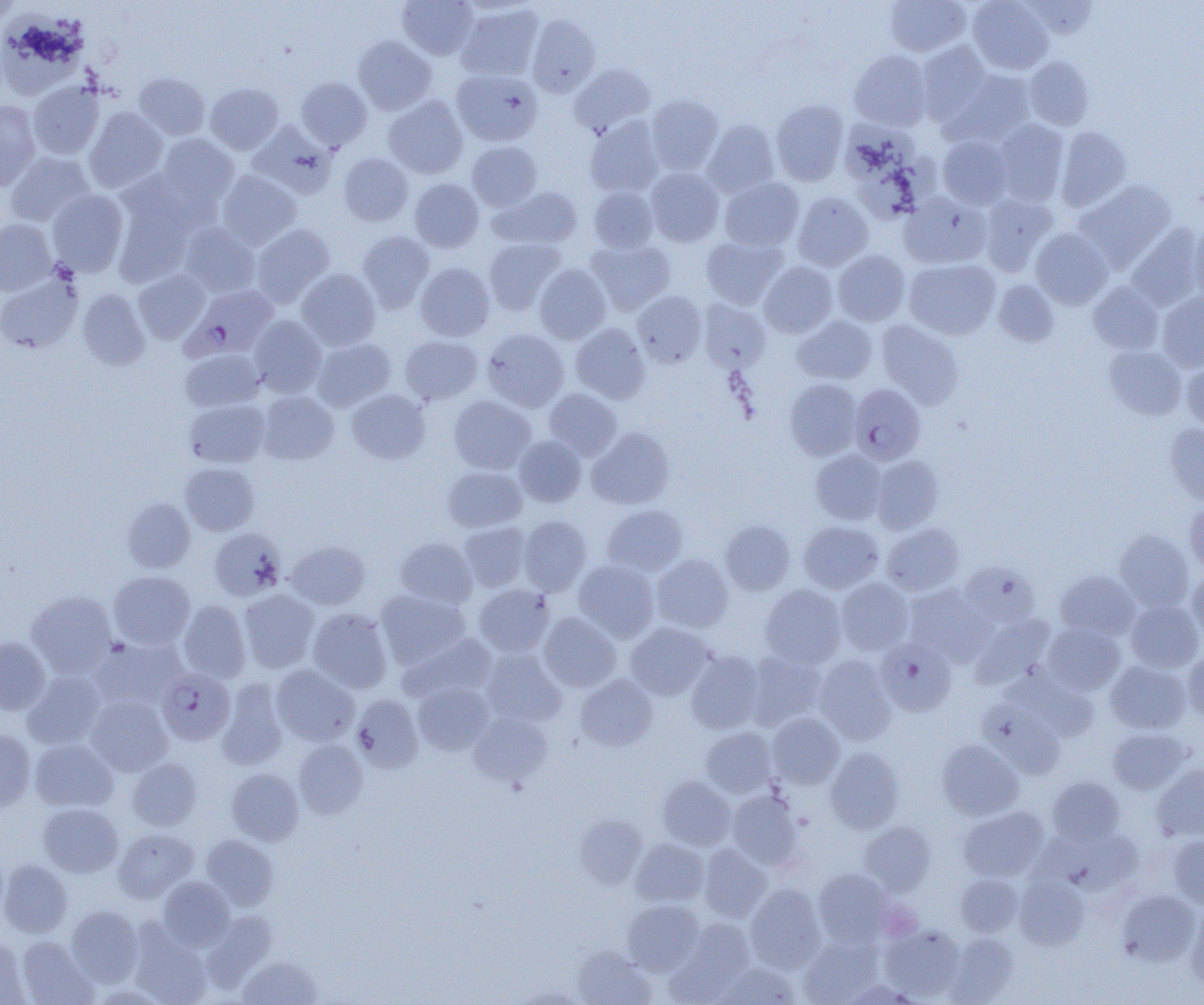
Plasmodium falciparum-infected red blood cell locations (subset) = approximate bounding boxes as (x1,y1)-(x2,y2) corner pairs in pixels: (175,289)-(282,368), (876,638)-(956,716), (156,668)-(235,746)
slide-level diagnosis = Plasmodium falciparum
image size = 1204×1005 pixels
uninfected red blood cell locations (subset) = approximate bounding boxes as (x1,y1)-(x2,y2) corner pairs in pixels: (397,0)-(478,60), (884,0)-(971,56), (967,0)-(1052,74), (1021,1)-(1098,39), (455,3)-(543,81), (0,13)-(88,99), (527,14)-(600,97), (353,36)-(437,115), (916,41)-(992,124), (849,50)-(932,131), (1024,56)-(1094,130), (569,64)-(655,137), (452,69)-(543,146), (947,70)-(1036,146), (134,73)-(210,140), (296,77)-(372,149), (27,81)-(104,159), (205,83)-(284,154), (646,95)-(723,174), (384,96)-(468,178), (770,99)-(848,186), (0,100)-(41,191), (84,107)-(168,192), (585,116)-(664,197), (702,119)-(780,197), (994,119)-(1069,205), (249,122)-(337,197), (840,122)-(919,182), (1056,126)-(1131,211), (155,134)-(238,211), (937,135)-(1013,209), (467,141)-(542,211), (5,152)-(95,228), (339,153)-(413,226), (851,153)-(940,222), (646,167)-(724,247), (217,170)-(302,250), (719,177)-(804,251), (409,178)-(484,253), (1075,180)-(1177,271), (589,186)-(659,253), (490,187)-(583,249), (47,189)-(128,276), (112,192)-(195,288), (792,192)-(873,271), (899,192)-(991,269), (980,193)-(1057,275), (1191,218)-(1204,305), (0,219)-(56,295), (179,223)-(260,298), (250,224)-(335,307), (1127,224)-(1203,312), (1030,228)-(1113,309), (357,231)-(435,312), (701,236)-(787,309), (484,238)-(565,315), (586,239)-(676,315), (833,250)-(910,326), (904,259)-(1000,340), (759,262)-(838,337), (415,263)-(495,341), (534,264)-(611,344), (296,268)-(381,351), (133,270)-(210,344), (0,274)-(82,353), (993,280)-(1060,347), (1088,281)-(1164,355), (78,288)-(150,369), (633,291)-(707,367), (1157,292)-(1204,371), (698,300)-(771,372), (792,315)-(877,385), (248,316)-(327,398), (876,320)-(964,409), (571,323)-(651,403), (482,328)-(569,412), (400,335)-(483,405), (311,337)-(396,411), (1104,346)-(1187,420), (180,349)-(264,412), (1182,360)-(1204,434), (784,379)-(862,460), (347,389)-(431,464), (544,389)-(622,460), (258,391)-(339,465), (449,395)-(536,474), (184,398)-(270,468), (1164,423)-(1204,506), (587,427)-(674,509), (514,436)-(586,507), (811,449)-(888,525), (871,455)-(944,535), (180,462)-(259,535), (443,466)-(527,532), (122,498)-(195,572), (1184,503)-(1204,575), (602,505)-(688,576), (519,515)-(592,595), (720,520)-(795,595), (798,521)-(883,593), (459,522)-(531,591), (882,523)-(965,596), (209,528)-(286,601), (1114,529)-(1195,612), (210,533)-(367,604), (394,537)-(478,609), (285,540)-(370,610), (652,554)-(733,633), (573,560)-(660,642), (959,562)-(1041,630), (1055,570)-(1141,640), (109,571)-(195,649), (1186,571)-(1204,640), (836,578)-(914,655), (905,584)-(995,666), (474,585)-(555,657), (760,585)-(846,668), (239,589)-(319,673), (375,590)-(470,669), (26,591)-(118,677), (178,599)-(251,683), (1126,600)-(1203,672), (307,608)-(392,694), (539,612)-(621,692), (970,613)-(1056,689), (626,623)-(714,700), (1042,623)-(1125,695), (399,633)-(496,704), (0,637)-(51,714), (90,637)-(187,709), (482,649)-(566,727), (744,650)-(826,729), (1183,650)-(1204,720), (686,651)-(765,734), (813,655)-(896,745), (1105,660)-(1191,733), (271,664)-(359,746), (1003,665)-(1100,740), (22,671)-(106,750), (576,675)-(657,751), (216,679)-(289,770), (413,682)-(492,755), (352,694)-(425,773), (86,695)-(173,775), (979,699)-(1066,779), (469,711)-(553,787), (768,713)-(845,789), (700,727)-(778,798), (1107,727)-(1194,794), (0,729)-(36,811), (30,739)-(118,812), (294,739)-(367,819), (936,739)-(1023,820), (825,746)-(904,834), (127,758)-(202,831), (1151,764)-(1204,842), (227,768)-(304,845), (657,776)-(736,850), (1047,776)-(1125,846), (727,790)-(803,869), (38,804)-(124,877), (958,806)-(1050,882), (574,814)-(647,889), (859,821)-(936,896), (113,827)-(198,902), (201,834)-(279,910), (1167,835)-(1204,908), (630,838)-(709,907), (699,844)-(772,921), (0,859)-(72,937), (813,868)-(893,947), (955,873)-(1023,937), (1014,874)-(1089,950), (158,876)-(234,950), (745,884)-(826,973), (1116,890)-(1200,966), (623,900)-(705,975), (65,905)-(143,986), (1186,905)-(1204,993), (202,911)-(277,990), (665,919)-(755,1003), (880,924)-(965,1001), (129,928)-(211,1005), (943,933)-(1018,1004), (0,935)-(29,1005), (799,935)-(881,1004), (15,936)-(97,1005), (573,947)-(655,1005), (238,955)-(323,1004), (716,962)-(799,1004), (841,979)-(920,1004), (513,986)-(589,1004)
modality = optical microscopy
preparation = thin blood film
platelet locations = approximate bounding boxes as (x1,y1)-(x2,y2) corner pairs in pixels: (882,903)-(925,943)
magnification = 1000x
field of view = one of a larger specimen